Identify the parasite.
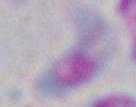
Toxoplasma gondii.

Photomicrograph. 1000x magnification.